Assess this cell for malaria.
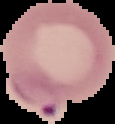

It is parasitized.

preparation = thin blood film
image type = segmented cell region on a black background
image size = 115×124 pixels